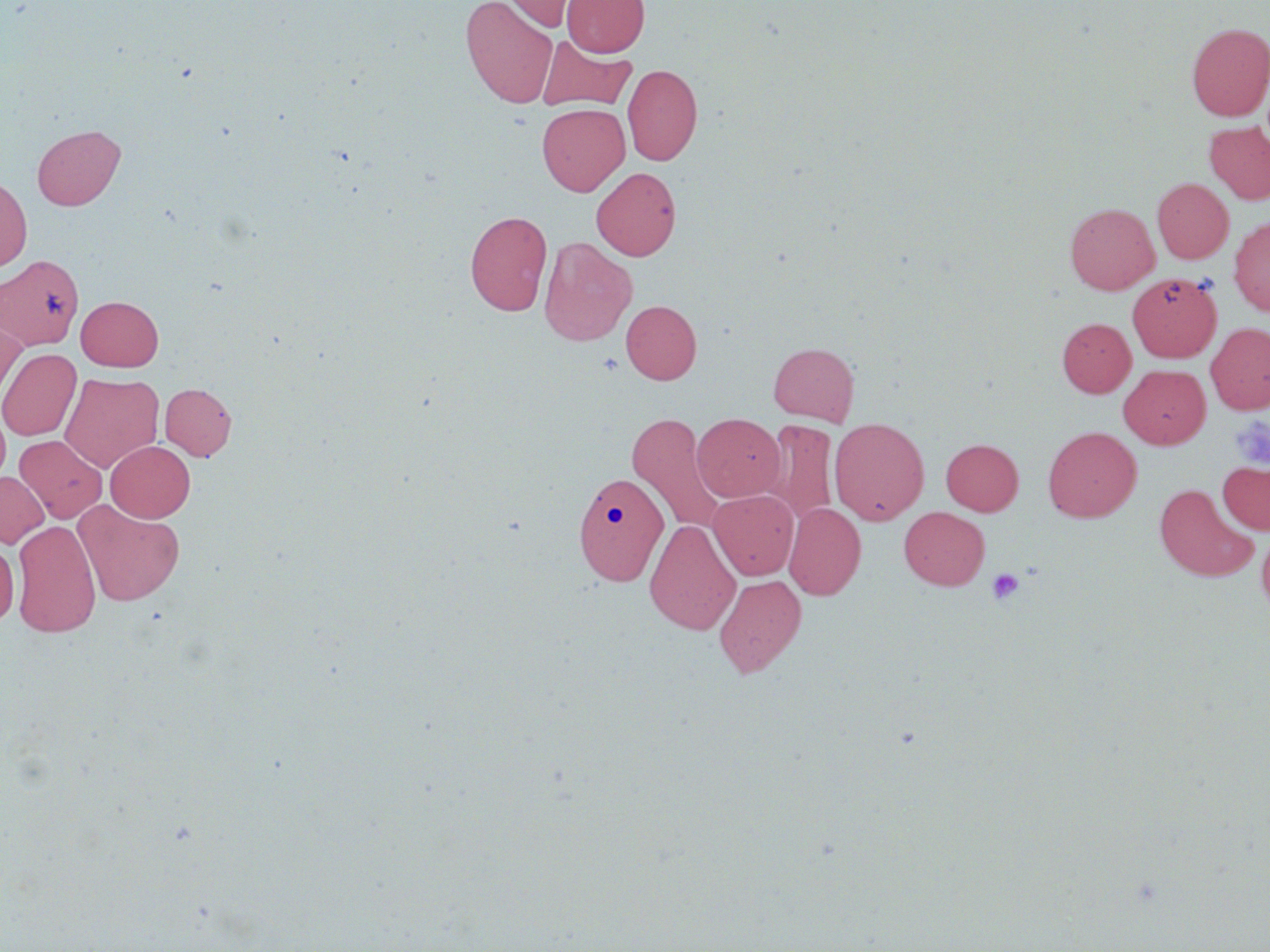
Approximate bounding boxes as named x1/y1/x2/y2 corners in pixels. Platelet locations: (x1=1230, y1=414, x2=1270, y2=471), (x1=987, y1=568, x2=1024, y2=605). Uninfected red blood cell locations: (x1=460, y1=0, x2=558, y2=108), (x1=499, y1=0, x2=593, y2=31), (x1=562, y1=0, x2=649, y2=57), (x1=1186, y1=23, x2=1270, y2=121), (x1=536, y1=35, x2=637, y2=113), (x1=622, y1=63, x2=703, y2=166), (x1=537, y1=103, x2=630, y2=196), (x1=1204, y1=121, x2=1270, y2=205), (x1=32, y1=124, x2=126, y2=210), (x1=591, y1=167, x2=681, y2=261), (x1=0, y1=175, x2=32, y2=272), (x1=1152, y1=177, x2=1233, y2=264), (x1=1065, y1=202, x2=1159, y2=294), (x1=465, y1=210, x2=552, y2=316), (x1=1229, y1=217, x2=1270, y2=316), (x1=539, y1=236, x2=638, y2=347), (x1=1, y1=254, x2=84, y2=352), (x1=1127, y1=273, x2=1221, y2=361), (x1=76, y1=296, x2=163, y2=371), (x1=620, y1=300, x2=702, y2=384), (x1=0, y1=312, x2=27, y2=405), (x1=1057, y1=318, x2=1136, y2=397), (x1=1205, y1=323, x2=1270, y2=415), (x1=768, y1=342, x2=859, y2=425), (x1=0, y1=348, x2=81, y2=441), (x1=1119, y1=364, x2=1210, y2=449), (x1=60, y1=372, x2=164, y2=473), (x1=160, y1=382, x2=237, y2=460), (x1=0, y1=408, x2=10, y2=487), (x1=627, y1=413, x2=727, y2=534), (x1=692, y1=413, x2=785, y2=502), (x1=829, y1=417, x2=930, y2=525), (x1=764, y1=419, x2=839, y2=526), (x1=1043, y1=426, x2=1141, y2=522), (x1=15, y1=435, x2=107, y2=523), (x1=941, y1=439, x2=1023, y2=515), (x1=105, y1=440, x2=195, y2=522), (x1=1217, y1=459, x2=1270, y2=535), (x1=0, y1=471, x2=49, y2=548), (x1=574, y1=472, x2=668, y2=585), (x1=1154, y1=483, x2=1259, y2=582), (x1=708, y1=489, x2=799, y2=580), (x1=73, y1=499, x2=185, y2=606), (x1=784, y1=502, x2=866, y2=600), (x1=899, y1=507, x2=990, y2=590), (x1=645, y1=519, x2=741, y2=635), (x1=12, y1=520, x2=101, y2=637), (x1=1256, y1=521, x2=1270, y2=616), (x1=0, y1=540, x2=19, y2=627), (x1=714, y1=574, x2=807, y2=678). Slide-level diagnosis: no evidence of blood parasites. Image is 1270×952 pixels. Optical microscopy. 1000x magnification. Thin blood smear. May-Grünwald-Giemsa-stained preparation. Single field of view.